Assess the morphology of the erythrocytes.
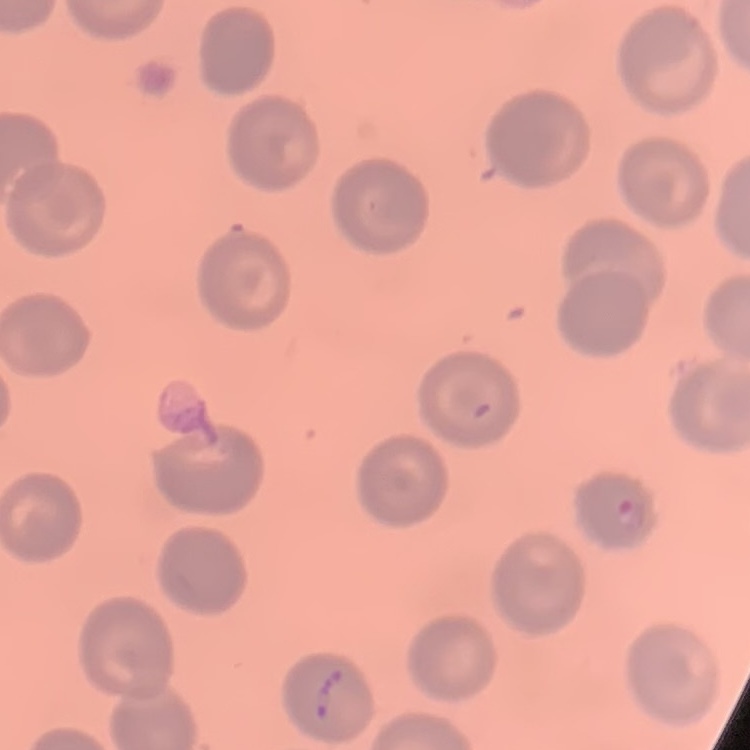
No rouleaux formation.

Thin peripheral smear. Field's or Giemsa stain. Square crop of a larger photomicrograph.